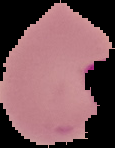

Summary:
  - Image size: 115×148 pixels
  - Malaria status: parasitized
  - Preparation: thin blood smear
  - Image type: segmented cell region on a black background